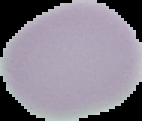
Summary:
  - Image type: segmented cell region on a black background
  - Malaria status: uninfected
  - Preparation: thin blood film
  - Image size: 142×121 pixels